Report the malaria status of this cell.
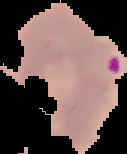

Parasitized.

{
  "preparation": "thin blood film",
  "image_type": "cell region segmented out of the field of view; surrounding area masked to black",
  "image_size": "127×154 pixels"
}